Identify the parasite.
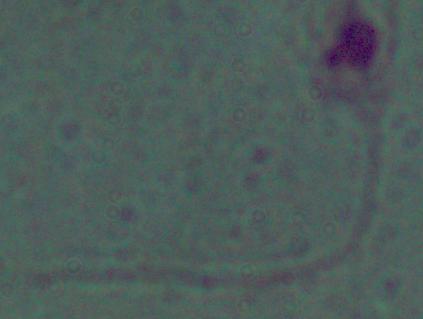
Leishmania.

1000x magnification. Micrograph.